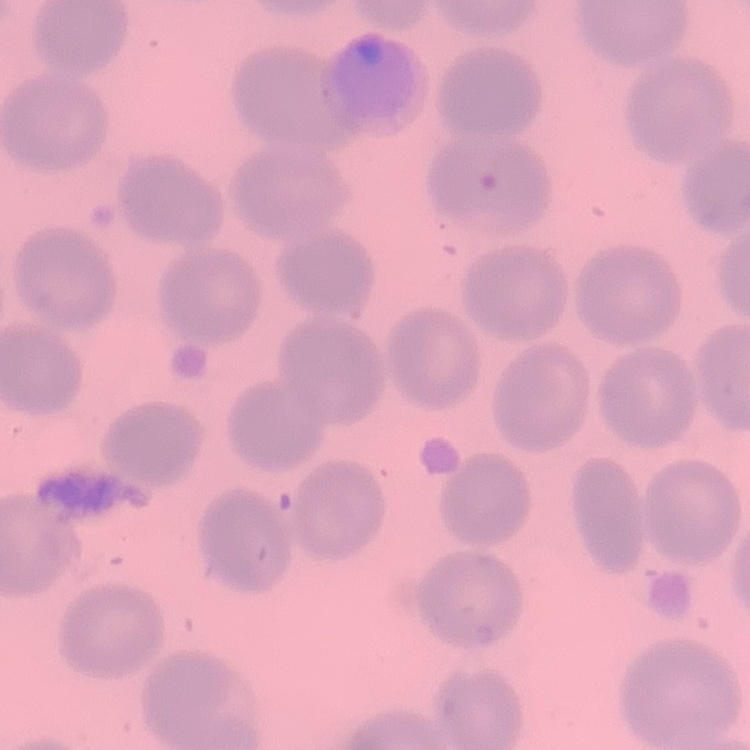

red_blood_cell_morphology: no rouleaux formation
preparation: thin peripheral smear
stain: Field's or Giemsa
image_type: square crop of a larger photomicrograph